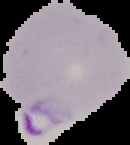

Summary:
  - Result: Plasmodium parasites detected
  - Preparation: thin blood film
  - Image type: segmented cell region on a black background
  - Image size: 130×145 pixels